State which parasite is depicted.
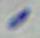
This is Toxoplasma gondii.

modality = photomicrograph
magnification = 1000x